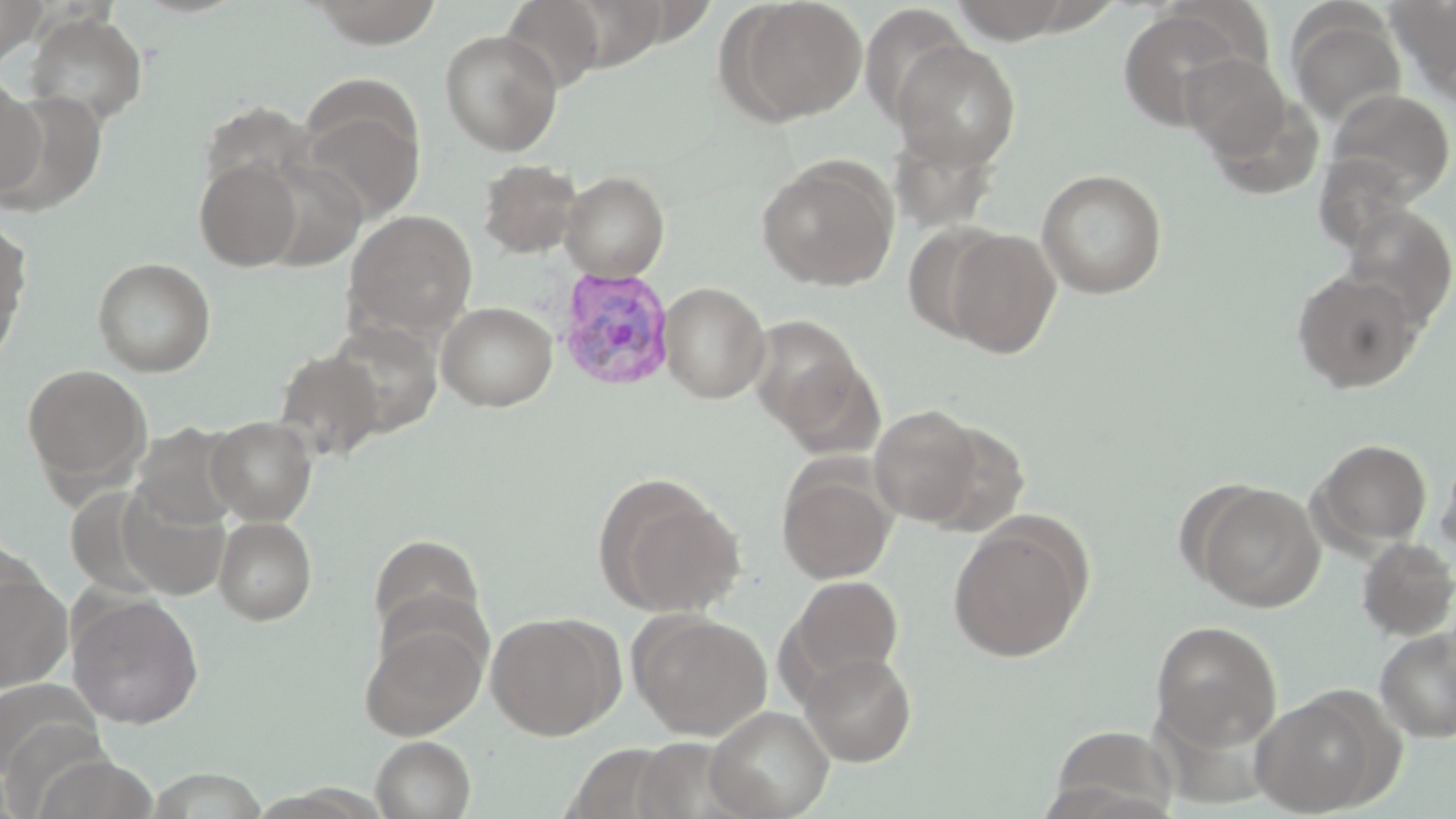

Summary:
  - Coordinate format: approximate bounding boxes as named x1/y1/x2/y2 corners in pixels
  - Plasmodium vivax-infected red blood cell locations: (x1=555, y1=267, x2=675, y2=393)
  - Uninfected red blood cell locations: (x1=0, y1=0, x2=50, y2=66), (x1=498, y1=0, x2=608, y2=93), (x1=725, y1=0, x2=867, y2=123), (x1=1385, y1=0, x2=1456, y2=93), (x1=308, y1=1, x2=444, y2=48), (x1=859, y1=4, x2=971, y2=128), (x1=1116, y1=5, x2=1257, y2=129), (x1=25, y1=11, x2=148, y2=127), (x1=1287, y1=11, x2=1406, y2=128), (x1=439, y1=29, x2=562, y2=155), (x1=891, y1=40, x2=1022, y2=171), (x1=1180, y1=53, x2=1293, y2=164), (x1=0, y1=69, x2=44, y2=199), (x1=1325, y1=88, x2=1455, y2=207), (x1=296, y1=95, x2=425, y2=224), (x1=886, y1=124, x2=1001, y2=232), (x1=256, y1=155, x2=368, y2=271), (x1=755, y1=156, x2=898, y2=292), (x1=194, y1=158, x2=303, y2=271), (x1=478, y1=159, x2=582, y2=258), (x1=1036, y1=169, x2=1168, y2=298), (x1=561, y1=171, x2=670, y2=281), (x1=1341, y1=205, x2=1456, y2=330), (x1=343, y1=209, x2=478, y2=339), (x1=0, y1=219, x2=32, y2=356), (x1=903, y1=220, x2=1013, y2=343), (x1=943, y1=228, x2=1062, y2=359), (x1=92, y1=256, x2=216, y2=376), (x1=1291, y1=269, x2=1422, y2=393), (x1=659, y1=281, x2=771, y2=404), (x1=437, y1=301, x2=557, y2=411), (x1=747, y1=313, x2=870, y2=444), (x1=324, y1=320, x2=443, y2=437), (x1=273, y1=348, x2=384, y2=461), (x1=20, y1=363, x2=153, y2=494), (x1=869, y1=404, x2=984, y2=526), (x1=206, y1=416, x2=317, y2=524), (x1=909, y1=419, x2=1029, y2=536), (x1=129, y1=423, x2=244, y2=531), (x1=1312, y1=438, x2=1432, y2=548), (x1=1435, y1=444, x2=1456, y2=566), (x1=776, y1=463, x2=896, y2=584), (x1=594, y1=474, x2=747, y2=619), (x1=1191, y1=481, x2=1323, y2=612), (x1=213, y1=516, x2=317, y2=624), (x1=948, y1=520, x2=1089, y2=663), (x1=369, y1=533, x2=485, y2=642), (x1=1356, y1=537, x2=1456, y2=640), (x1=0, y1=568, x2=73, y2=693), (x1=787, y1=575, x2=904, y2=690), (x1=67, y1=593, x2=204, y2=728), (x1=630, y1=611, x2=772, y2=740), (x1=485, y1=613, x2=621, y2=740), (x1=359, y1=617, x2=488, y2=741), (x1=1149, y1=620, x2=1283, y2=752), (x1=1374, y1=626, x2=1456, y2=742), (x1=800, y1=651, x2=917, y2=766), (x1=1251, y1=690, x2=1394, y2=816), (x1=705, y1=705, x2=834, y2=819), (x1=370, y1=735, x2=475, y2=818)
  - Slide-level diagnosis: Plasmodium vivax
  - Magnification: 1000x
  - Stain: May-Grünwald-Giemsa
  - Image size: 1456×819 pixels
  - Preparation: thin blood film
  - Modality: light microscopy
  - Field of view: one of a larger specimen